Give the location of every parasitized red blood cell.
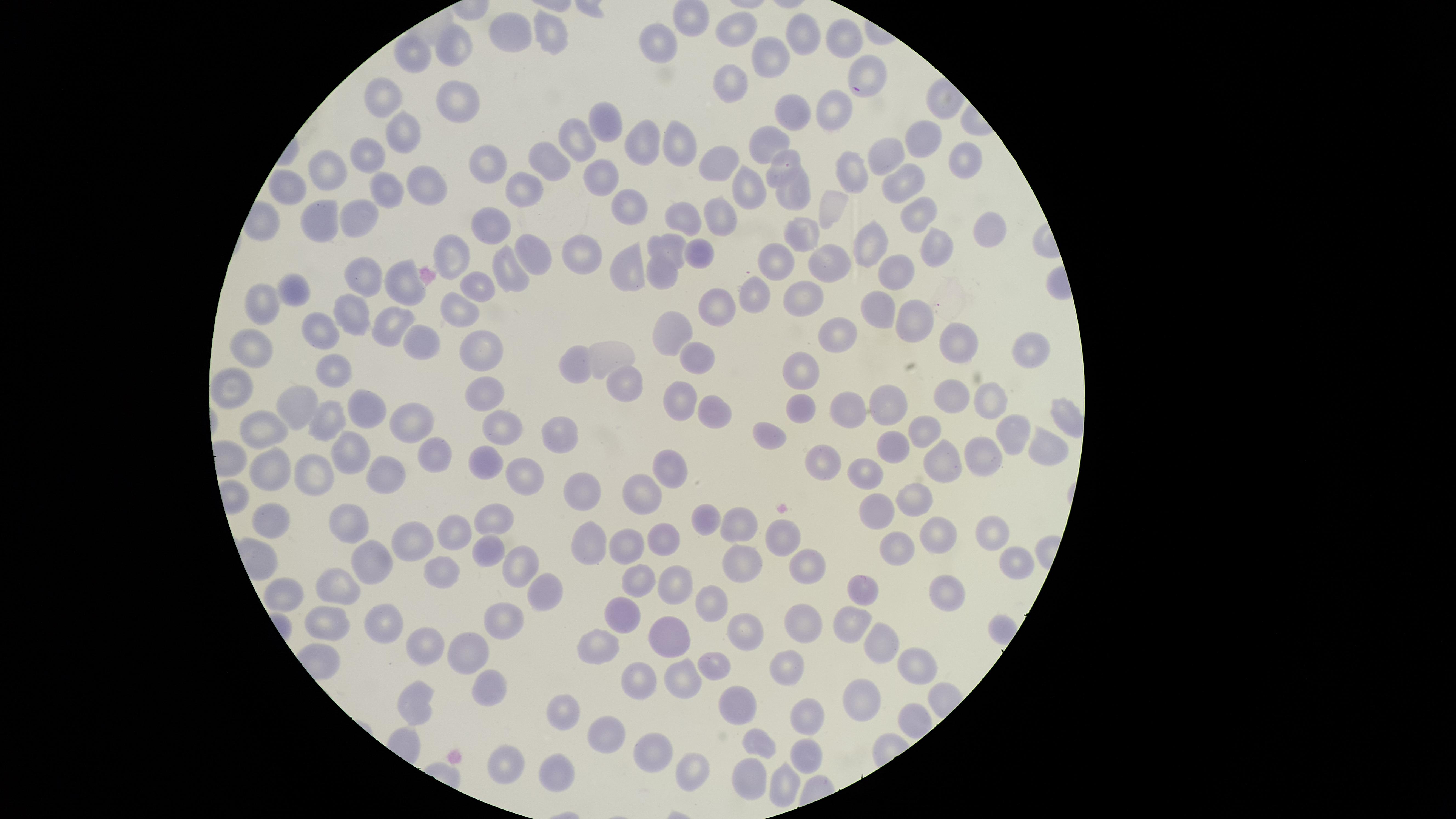

No parasitized red blood cells identified.

visible_region: circular
capture: smartphone photograph through the microscope eyepiece
image_size: 1456×819 pixels
field_of_view: single
preparation: thin blood smear
uninfected_red_blood_cells: 'approximate marker points as (x, y) in pixels: (737, 26), (511, 32), (552, 33), (798, 35), (845, 39), (461, 42), (664, 43), (419, 54), (777, 61), (865, 80), (727, 82), (459, 96), (382, 100), (837, 109), (790, 110), (606, 122), (403, 132), (927, 135), (644, 140), (770, 140), (580, 143), (675, 143), (370, 152), (887, 155), (550, 157), (487, 160), (714, 161), (964, 161), (788, 162), (859, 169), (323, 174), (601, 183), (423, 184), (756, 185), (903, 185), (291, 186), (387, 186), (528, 191), (791, 194), (632, 207), (831, 208), (719, 214), (356, 217), (321, 218), (683, 219), (913, 219), (498, 224), (990, 231), (809, 238), (864, 245), (704, 248), (937, 248), (668, 249), (533, 251), (586, 252), (454, 257), (831, 265), (628, 267), (780, 267), (902, 267), (516, 273), (665, 276), (364, 277), (400, 286), (477, 287), (758, 289), (299, 290), (811, 295), (262, 302), (880, 302), (719, 307), (457, 312), (351, 314), (914, 320), (395, 325), (324, 330), (674, 331), (836, 334), (422, 340), (953, 342), (486, 350), (253, 351), (613, 355), (1026, 355), (694, 357), (572, 363), (333, 367), (797, 368), (235, 384), (625, 387), (491, 390), (957, 396), (898, 402), (684, 403), (361, 404), (991, 404), (300, 405), (806, 406), (853, 411), (716, 418), (326, 419), (412, 424), (267, 426), (1014, 429), (926, 430), (504, 433), (560, 434), (772, 438), (896, 441), (1051, 451), (344, 452), (439, 453), (984, 454), (493, 459), (947, 459), (818, 463), (668, 464), (273, 468), (383, 472), (528, 472), (869, 472), (317, 478), (585, 490), (644, 493), (917, 497), (875, 509), (492, 514), (273, 517), (705, 520), (454, 525), (738, 525), (349, 527), (989, 533), (780, 535), (939, 535), (662, 539), (591, 541), (410, 542), (626, 544), (894, 546), (485, 552), (1011, 559), (742, 562), (803, 562), (518, 563), (439, 565), (370, 567), (635, 577), (675, 583), (339, 585), (953, 591), (867, 594), (539, 595), (287, 597), (712, 603), (624, 616), (329, 621), (503, 621), (744, 621), (852, 621), (802, 623), (376, 624), (666, 636), (881, 640), (426, 641), (601, 644), (473, 650), (915, 661), (714, 667), (784, 669), (679, 676), (633, 678), (487, 685), (866, 697), (418, 700), (567, 706), (742, 709), (807, 716), (606, 733), (763, 747), (660, 753), (806, 753), (502, 758), (692, 768), (557, 771), (753, 779), (784, 783)'
stain: Giemsa